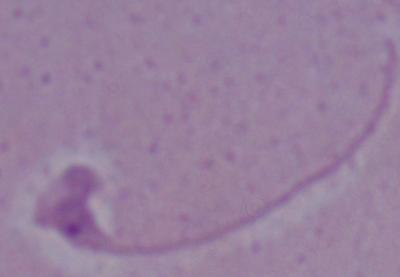

identification: Leishmania
modality: photomicrograph
magnification: 1000x